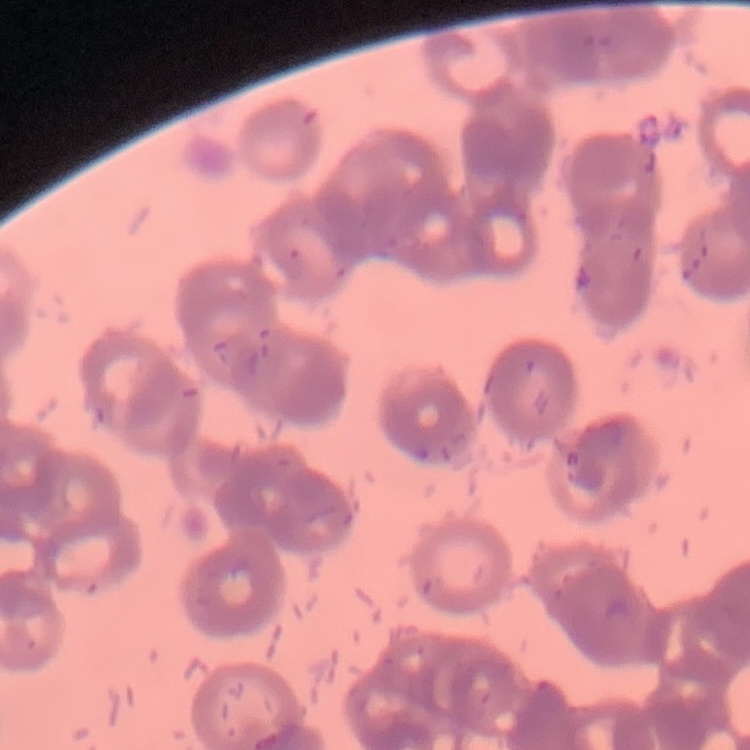
red blood cell morphology = rouleaux formation
preparation = thin blood film
stain = Field's or Giemsa
image type = one tile cut from a larger photomicrograph